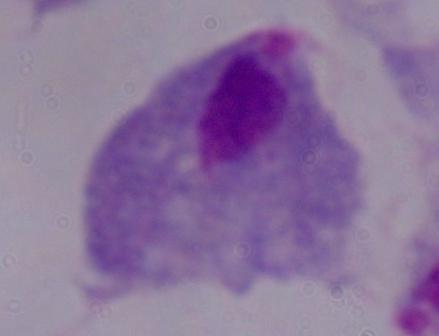

Summary:
  - Modality: photomicrograph
  - Magnification: 1000x
  - Identification: trichomonad